Assess the morphology of the red blood cells.
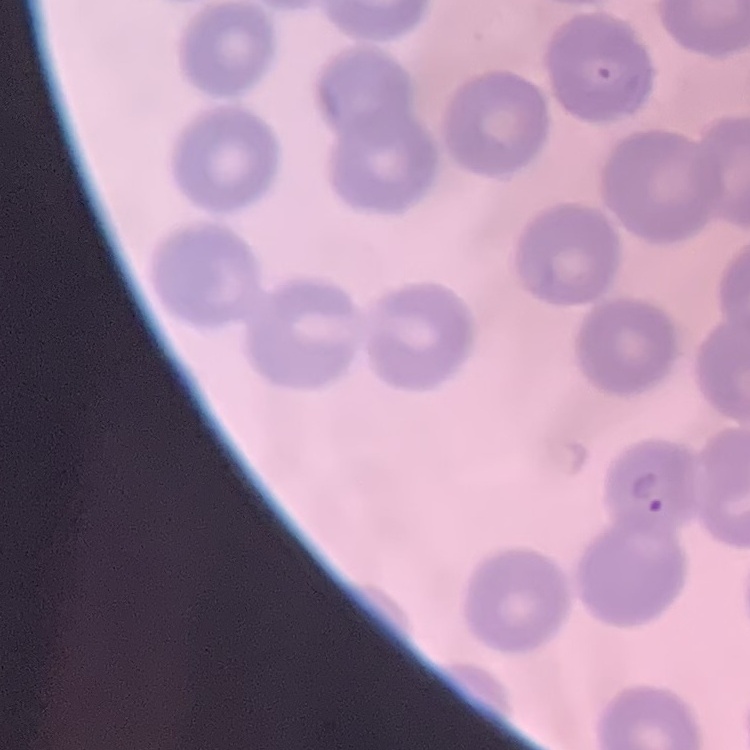
They show no rouleaux formation.

preparation: thin blood smear
image_type: square crop of a larger photomicrograph
stain: Field's or Giemsa